Classify this cell by malaria status.
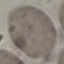

Uninfected.

{
  "capture": "smartphone through the microscope eyepiece",
  "preparation": "thin blood smear",
  "stain": "Giemsa",
  "image_type": "cell patch, automatically extracted from a larger field of view and resized to 64 × 64 pixels"
}